Outline each blood parasite and name the species.
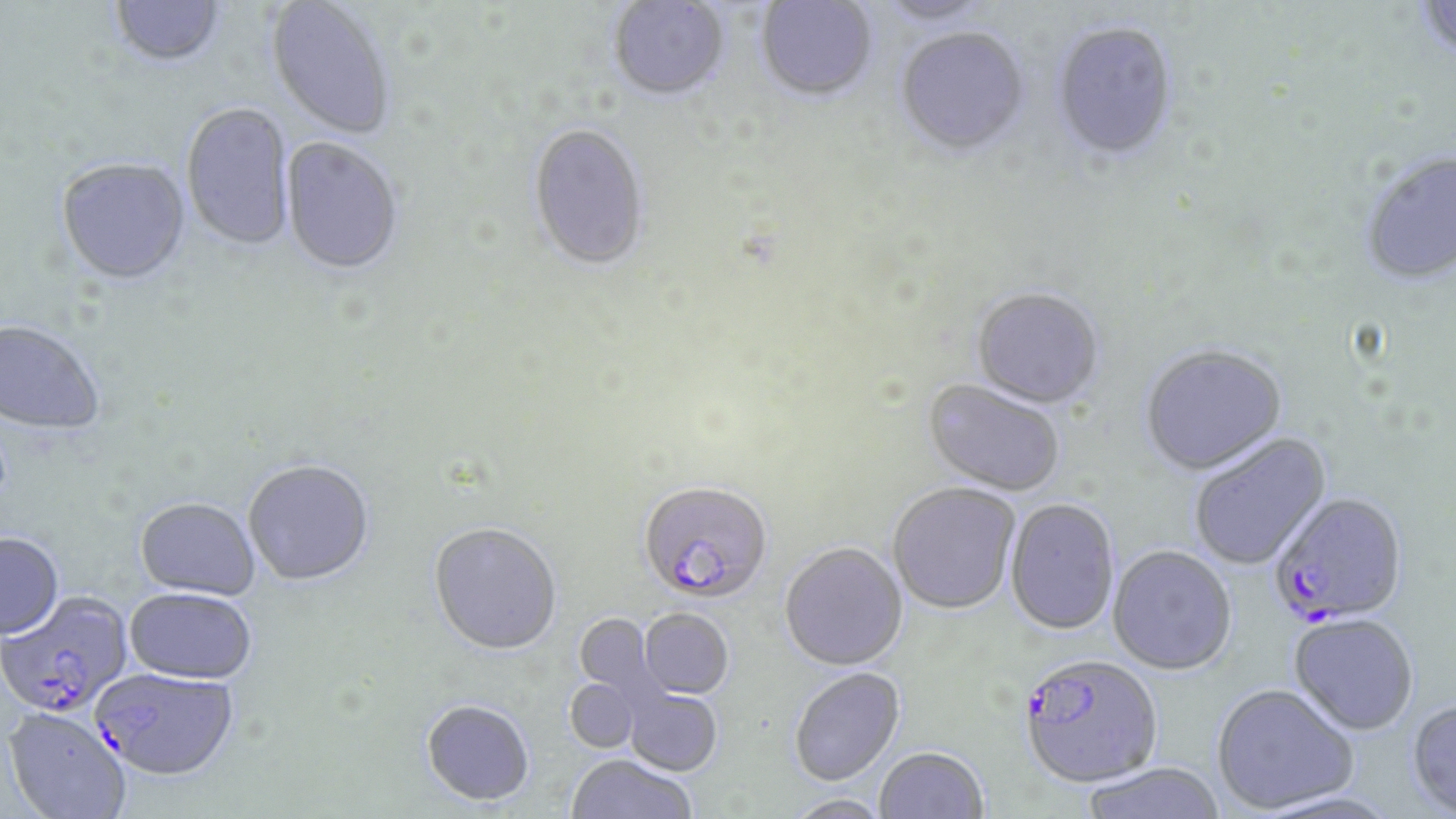
Approximate bounding boxes as (x1, y1, x2, y2) in pixels.
Plasmodium falciparum-infected red blood cells: (638, 482, 772, 606), (1270, 495, 1409, 628), (0, 592, 134, 721), (1024, 653, 1162, 790), (92, 668, 240, 782).
No Plasmodium ovale, Plasmodium malariae, Plasmodium vivax, Babesia divergens, or Trypanosoma brucei observed.

Uninfected red blood cell locations: (756, 0, 878, 104), (873, 0, 998, 28), (1415, 0, 1456, 64), (110, 1, 225, 70), (265, 1, 394, 142), (608, 1, 730, 104), (1052, 23, 1178, 163), (895, 29, 1029, 160), (181, 104, 296, 253), (528, 126, 649, 274), (281, 138, 404, 278), (1360, 151, 1456, 288), (55, 159, 192, 288), (971, 288, 1105, 411), (0, 321, 104, 437), (1141, 346, 1288, 478), (922, 380, 1064, 497), (1189, 432, 1333, 572), (243, 461, 375, 588), (888, 483, 1020, 614), (1005, 499, 1120, 636), (134, 500, 260, 602), (428, 525, 562, 657), (0, 534, 64, 642), (780, 542, 908, 670), (1107, 547, 1237, 676), (124, 590, 256, 687), (639, 609, 734, 699), (574, 613, 659, 701), (1288, 615, 1419, 737), (789, 667, 905, 785), (564, 679, 640, 753), (1211, 684, 1358, 814), (624, 687, 722, 776), (421, 699, 535, 806), (1406, 700, 1456, 818), (4, 710, 130, 819), (874, 746, 988, 819), (566, 754, 697, 819), (1080, 762, 1227, 819), (784, 794, 892, 818). Slide-level diagnosis: Plasmodium falciparum. One field of a larger specimen. May-Grünwald-Giemsa stain. Captured at 1000x magnification. Optical microscopy. Image is 1456×819 pixels. Thin blood smear.